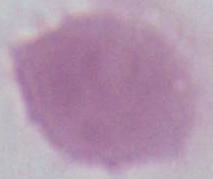
An erythrocyte is shown. Photomicrograph. Captured at 1000x magnification.